Give the position of every leukocyte visible.
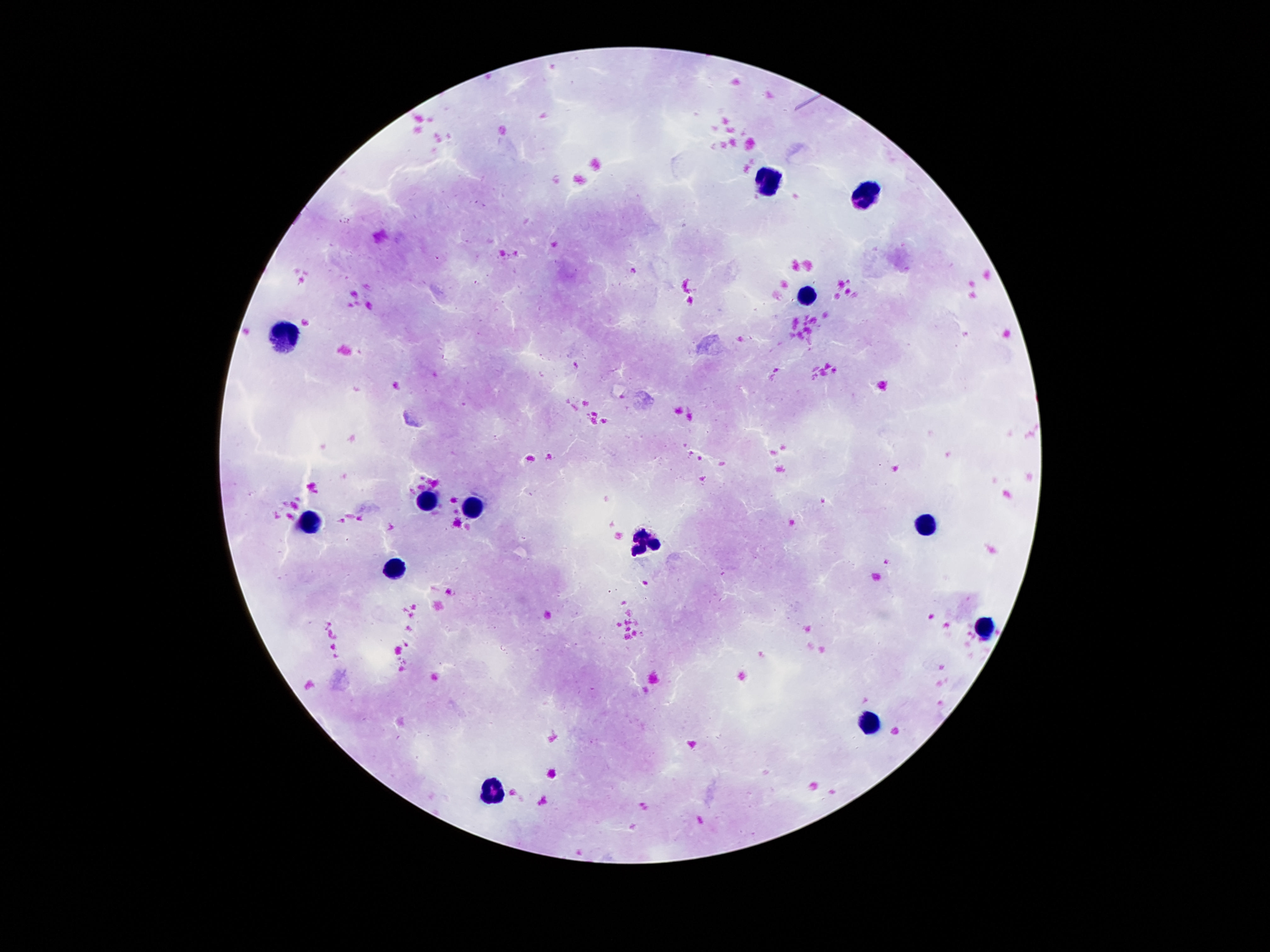

Approximate centers as {x, y} in pixels.
Leukocytes: {770, 181}, {863, 194}, {807, 293}, {289, 337}, {424, 500}, {471, 508}, {312, 521}, {928, 523}, {643, 543}, {396, 570}, {984, 627}, {870, 724}, {492, 789}.

stain: Giemsa
field_of_view: single
patient_malaria_status: uninfected
image_size: 1270×952 pixels
magnification: 100x
preparation: thick blood film
capture: smartphone camera through the microscope eyepiece